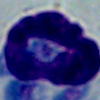

A leukocyte is shown. Micrograph. Captured at 1000x magnification.